Point out each Plasmodium parasite.
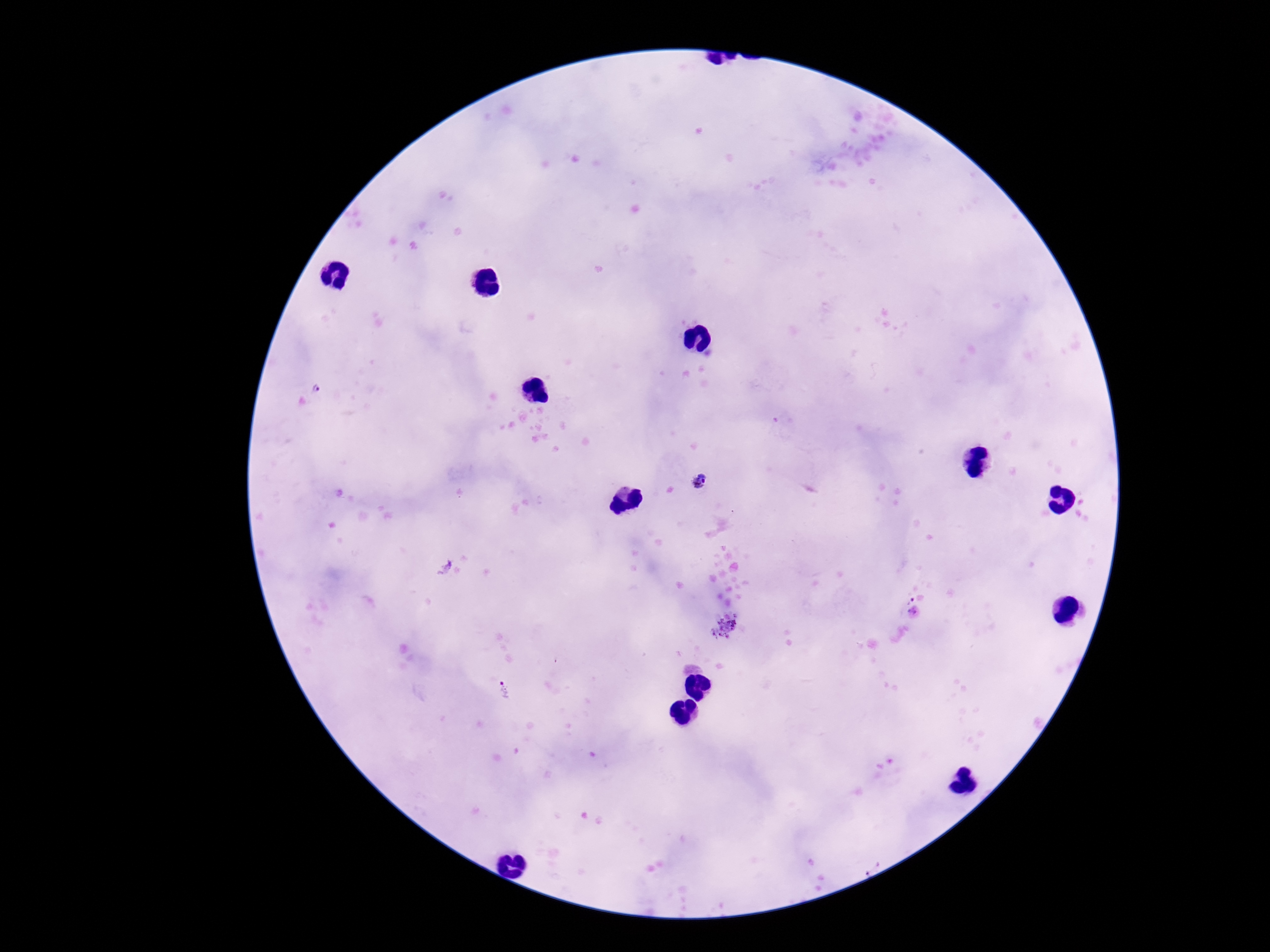

Approximate object centers, in pixels from the top-left corner.
Plasmodium parasites: (x=699, y=481), (x=724, y=631), (x=505, y=692).

field_of_view: single
preparation: thick blood film
magnification: 100x
capture: smartphone camera through the microscope eyepiece
stain: Giemsa
patient_malaria_status: positive
image_size: 1270×952 pixels